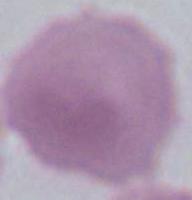 An erythrocyte is seen. 1000x magnification. Photomicrograph.